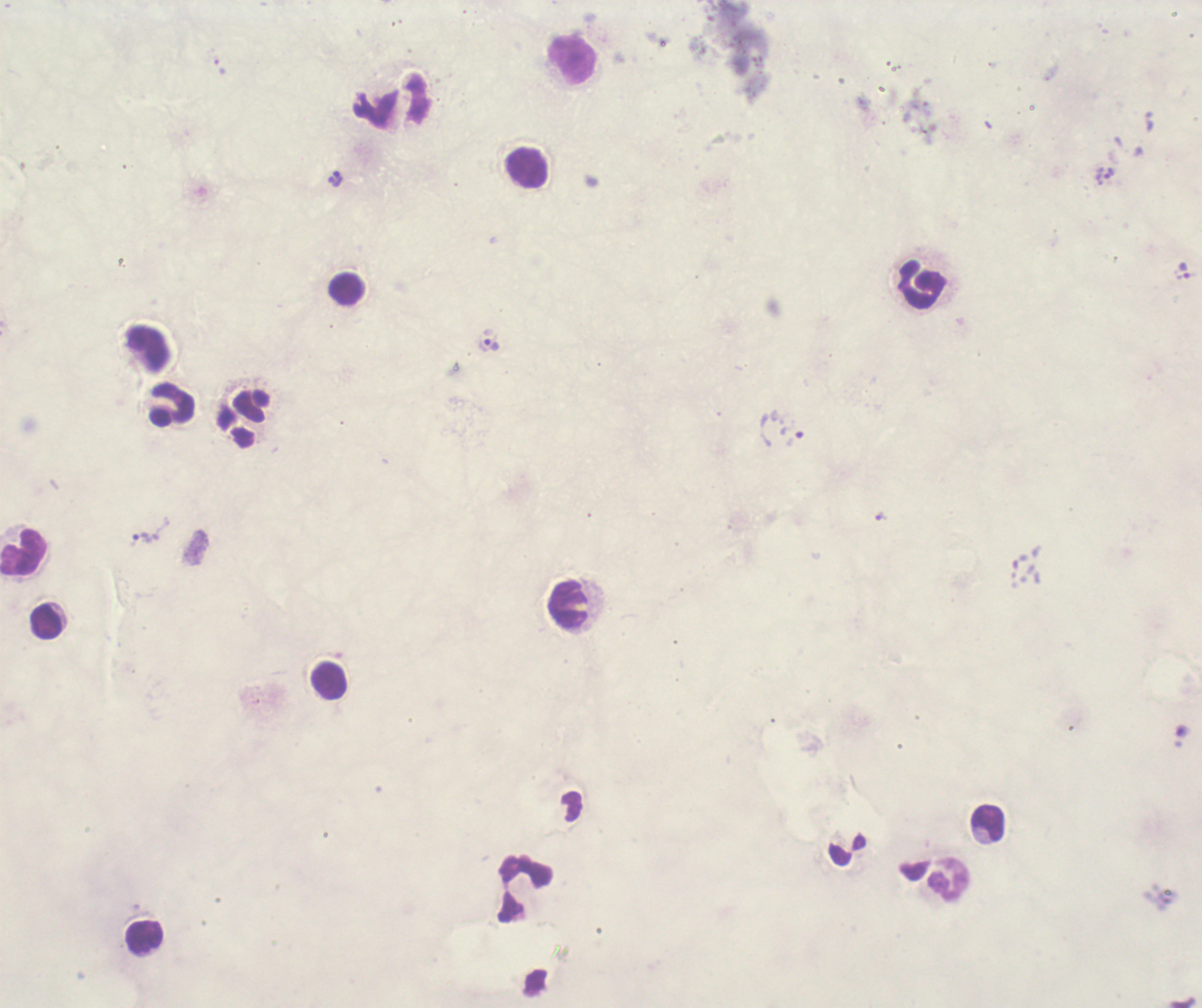
Approximate object centers, in pixels from the top-left corner.
Summary:
  - Leukocyte locations: (x=573, y=61), (x=528, y=168), (x=924, y=286), (x=344, y=289), (x=172, y=404), (x=24, y=554), (x=570, y=605), (x=46, y=622), (x=330, y=683), (x=988, y=824), (x=950, y=879), (x=526, y=889), (x=144, y=938)
  - Trophozoite locations: (x=1110, y=174), (x=336, y=179), (x=1185, y=271), (x=492, y=345), (x=794, y=439), (x=145, y=537)
  - Image size: 1202×1008 pixels
  - Preparation: thick blood smear
  - Coloration quality: bad
  - Magnification: 100x
  - Result: positive for Plasmodium parasites
  - Stain: Romanowsky
  - Context: previously used in an actual diagnosis
  - Background quality: unsatisfactory
  - Field of view: single